Describe the morphology of the erythrocytes.
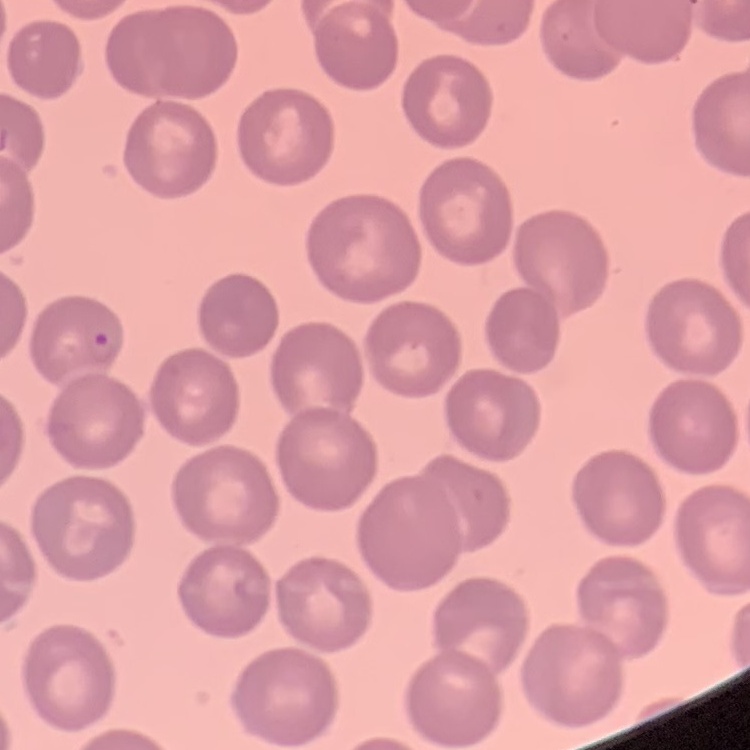

They show no rouleaux formation.

Thin blood film. Stained with either Field's or Giemsa. Square crop of a larger photomicrograph.